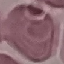

result = negative for malaria parasites
preparation = thin blood smear
capture = smartphone camera at the microscope eyepiece
stain = Giemsa
image type = cell patch, automatically extracted from a larger field of view and resized to 64 × 64 pixels